Describe the morphology of the red blood cells.
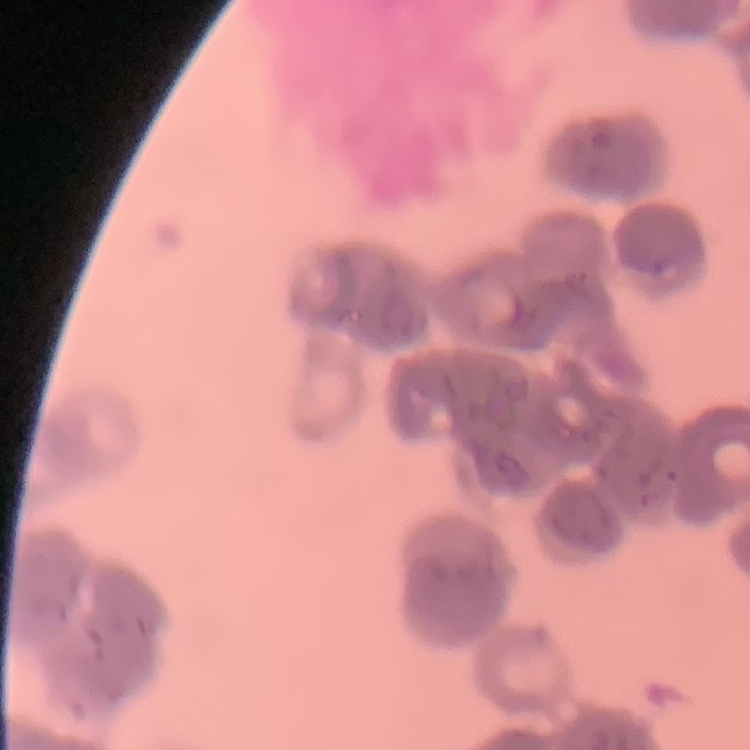
Rouleaux formation.

image type = square crop of a larger photomicrograph
preparation = thin blood smear
stain = Field's or Giemsa